State which parasite is depicted.
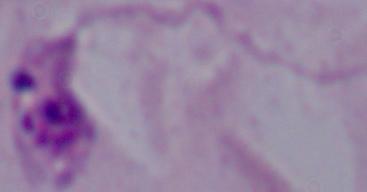
Leishmania.

Summary:
  - Modality: micrograph
  - Magnification: 1000x